Give the extent of all Plasmodium vivax-infected red blood cells.
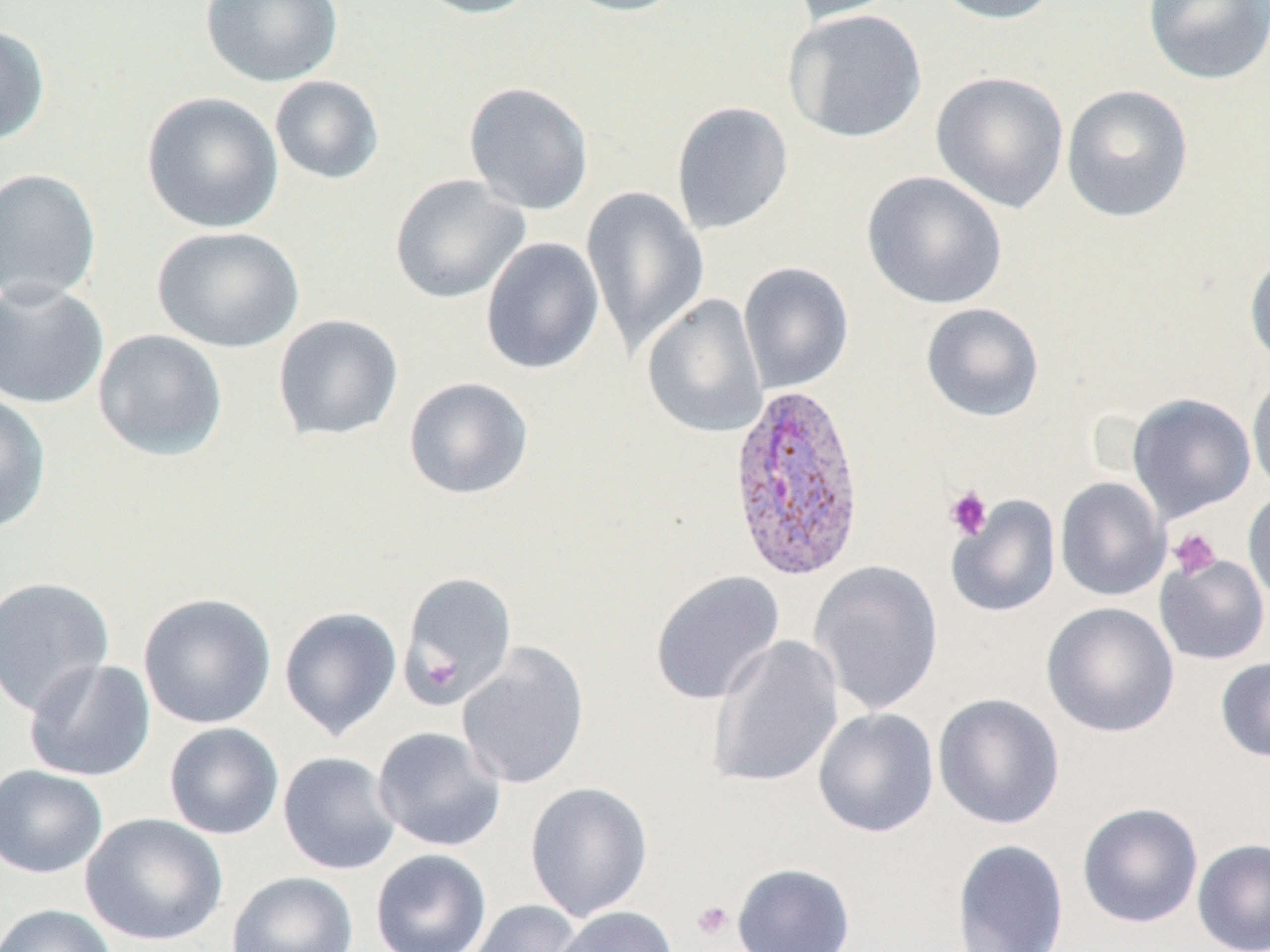
Approximate bounding boxes as (x1, y1, x2, y2) in pixels.
Plasmodium vivax-infected red blood cells: (727, 380, 867, 583).

Platelet locations: (944, 485, 993, 540), (1168, 528, 1222, 580), (692, 900, 734, 940). Uninfected red blood cell locations: (201, 0, 344, 88), (412, 0, 546, 20), (557, 0, 689, 17), (783, 0, 905, 25), (929, 0, 1063, 25), (1143, 0, 1270, 85), (783, 8, 927, 144), (0, 23, 50, 148), (931, 71, 1070, 213), (269, 75, 385, 186), (463, 81, 595, 216), (1061, 84, 1194, 223), (141, 91, 284, 233), (671, 101, 794, 236), (0, 168, 102, 305), (861, 171, 1008, 310), (389, 174, 531, 304), (580, 185, 711, 354), (152, 226, 304, 353), (480, 237, 605, 375), (1245, 250, 1270, 369), (738, 262, 854, 394), (0, 279, 109, 410), (642, 294, 768, 439), (920, 302, 1045, 422), (272, 314, 404, 442), (92, 329, 229, 461), (1247, 370, 1270, 498), (403, 376, 535, 500), (0, 392, 51, 534), (1127, 393, 1256, 521), (1055, 476, 1170, 601), (1243, 486, 1270, 608), (947, 495, 1061, 617), (1154, 554, 1270, 665), (809, 560, 944, 716), (649, 570, 785, 706), (398, 571, 517, 707), (0, 576, 115, 718), (138, 592, 277, 729), (1041, 602, 1180, 738), (279, 606, 402, 740), (706, 635, 844, 788), (457, 644, 589, 790), (1215, 656, 1270, 762), (24, 658, 156, 782), (932, 693, 1065, 830), (813, 707, 939, 838), (163, 722, 284, 840), (372, 726, 506, 852), (277, 751, 401, 875), (0, 764, 108, 878), (524, 781, 654, 922), (1076, 802, 1204, 928), (80, 813, 228, 946), (1192, 838, 1270, 952), (951, 839, 1070, 952), (370, 848, 492, 952), (731, 862, 856, 952), (226, 871, 359, 952), (466, 900, 586, 952), (0, 903, 117, 952), (551, 907, 678, 952). Slide-level diagnosis: Plasmodium vivax. Captured at 1000x magnification. May-Grünwald-Giemsa-stained preparation. Single field of view. Image is 1270×952 pixels. Optical microscopy. Thin blood smear.